Outline each uninfected red blood cell.
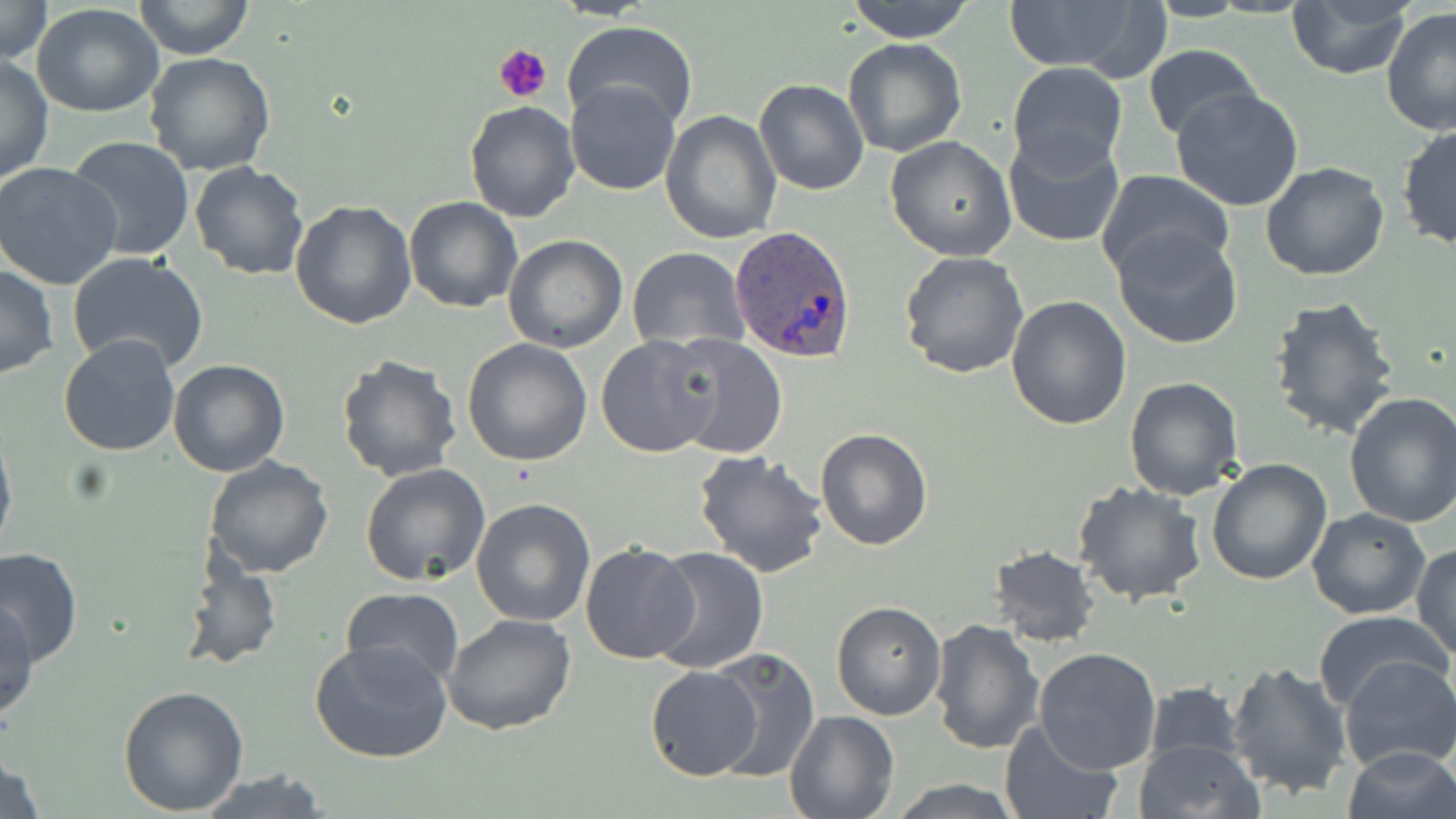
Approximate bounding boxes as named x1/y1/x2/y2 corners in pixels.
Uninfected red blood cells: (x1=0, y1=0, x2=52, y2=65), (x1=131, y1=0, x2=255, y2=61), (x1=845, y1=0, x2=977, y2=42), (x1=1002, y1=0, x2=1165, y2=79), (x1=1286, y1=1, x2=1417, y2=80), (x1=31, y1=4, x2=164, y2=116), (x1=1381, y1=7, x2=1456, y2=137), (x1=562, y1=21, x2=698, y2=132), (x1=842, y1=36, x2=967, y2=156), (x1=1141, y1=45, x2=1263, y2=145), (x1=144, y1=51, x2=276, y2=175), (x1=0, y1=53, x2=55, y2=185), (x1=1006, y1=62, x2=1128, y2=171), (x1=753, y1=79, x2=868, y2=196), (x1=564, y1=81, x2=682, y2=195), (x1=1170, y1=86, x2=1305, y2=212), (x1=464, y1=100, x2=581, y2=222), (x1=661, y1=111, x2=781, y2=245), (x1=1396, y1=124, x2=1455, y2=250), (x1=1002, y1=132, x2=1127, y2=248), (x1=885, y1=135, x2=1016, y2=260), (x1=65, y1=137, x2=197, y2=261), (x1=1260, y1=160, x2=1389, y2=281), (x1=190, y1=161, x2=308, y2=280), (x1=0, y1=162, x2=123, y2=289), (x1=1094, y1=168, x2=1232, y2=281), (x1=404, y1=195, x2=522, y2=312), (x1=290, y1=200, x2=417, y2=329), (x1=1112, y1=226, x2=1243, y2=349), (x1=503, y1=235, x2=629, y2=353), (x1=627, y1=248, x2=748, y2=350), (x1=900, y1=250, x2=1030, y2=378), (x1=66, y1=252, x2=209, y2=374), (x1=1, y1=263, x2=58, y2=380), (x1=1005, y1=295, x2=1132, y2=431), (x1=1267, y1=295, x2=1403, y2=442), (x1=668, y1=333, x2=786, y2=461), (x1=595, y1=334, x2=724, y2=458), (x1=58, y1=335, x2=182, y2=457), (x1=462, y1=337, x2=593, y2=466), (x1=334, y1=354, x2=461, y2=484), (x1=167, y1=358, x2=289, y2=476), (x1=1124, y1=375, x2=1246, y2=501), (x1=1344, y1=391, x2=1456, y2=527), (x1=0, y1=421, x2=17, y2=561), (x1=814, y1=426, x2=933, y2=549), (x1=692, y1=447, x2=829, y2=578), (x1=202, y1=454, x2=335, y2=578), (x1=1206, y1=459, x2=1331, y2=585), (x1=359, y1=463, x2=491, y2=587), (x1=1073, y1=483, x2=1207, y2=607), (x1=470, y1=496, x2=597, y2=627), (x1=1307, y1=507, x2=1432, y2=619), (x1=579, y1=542, x2=700, y2=665), (x1=0, y1=544, x2=82, y2=666), (x1=987, y1=544, x2=1101, y2=647), (x1=1412, y1=544, x2=1455, y2=659), (x1=179, y1=545, x2=283, y2=671), (x1=648, y1=546, x2=769, y2=674), (x1=340, y1=587, x2=465, y2=690), (x1=1, y1=600, x2=40, y2=723), (x1=830, y1=601, x2=945, y2=720), (x1=1315, y1=609, x2=1447, y2=710), (x1=443, y1=613, x2=577, y2=735), (x1=930, y1=618, x2=1045, y2=757), (x1=310, y1=637, x2=451, y2=763), (x1=1034, y1=648, x2=1163, y2=774), (x1=704, y1=649, x2=821, y2=780), (x1=1338, y1=657, x2=1456, y2=775), (x1=1225, y1=660, x2=1352, y2=801), (x1=645, y1=666, x2=763, y2=780), (x1=1142, y1=680, x2=1250, y2=768), (x1=117, y1=683, x2=250, y2=814), (x1=784, y1=711, x2=899, y2=819), (x1=999, y1=720, x2=1121, y2=819), (x1=1134, y1=739, x2=1264, y2=818), (x1=0, y1=744, x2=47, y2=819), (x1=1341, y1=745, x2=1455, y2=819), (x1=195, y1=767, x2=331, y2=819), (x1=888, y1=779, x2=1024, y2=817).

Plasmodium ovale-infected red blood cell locations = approximate bounding boxes as named x1/y1/x2/y2 corners in pixels: (x1=729, y1=227, x2=856, y2=363)
slide-level diagnosis = Plasmodium ovale
stain = May-Grünwald-Giemsa
modality = optical microscopy
field of view = single
magnification = 1000x
preparation = thin blood film
platelet locations = approximate bounding boxes as named x1/y1/x2/y2 corners in pixels: (x1=494, y1=44, x2=551, y2=103)
image size = 1456×819 pixels